Report the malaria status of this cell.
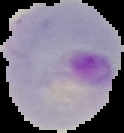

Parasitized.

Image is 124×133 pixels. The area outside the segmented cell region is set to black. From a thin blood smear.